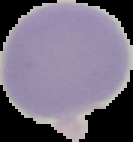 The area outside the segmented cell region is set to black. Image is 133×142 pixels. From a thin blood smear. Result: negative for Plasmodium parasites.